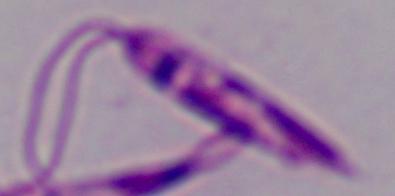

1000x magnification. A Leishmania parasite is seen. Photomicrograph.